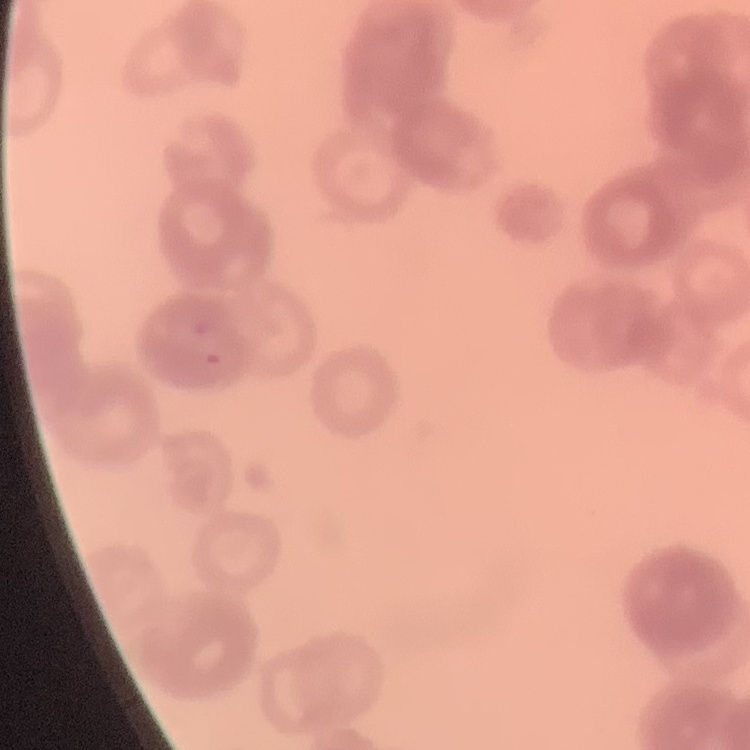
red blood cell morphology = rouleaux formation
image type = one tile cut from a larger photomicrograph
stain = Field's or Giemsa
preparation = thin blood film